Assess this cell for malaria.
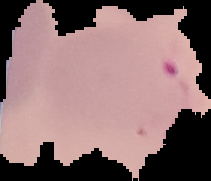
It is parasitized.

image_size: 211×181 pixels
preparation: thin blood smear
image_type: segmented cell region on a black background